State which cell type is depicted.
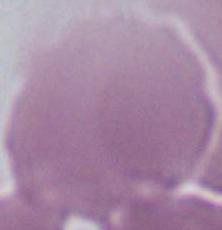
An erythrocyte.

Micrograph. Captured at 1000x magnification.